Locate and identify every blood parasite.
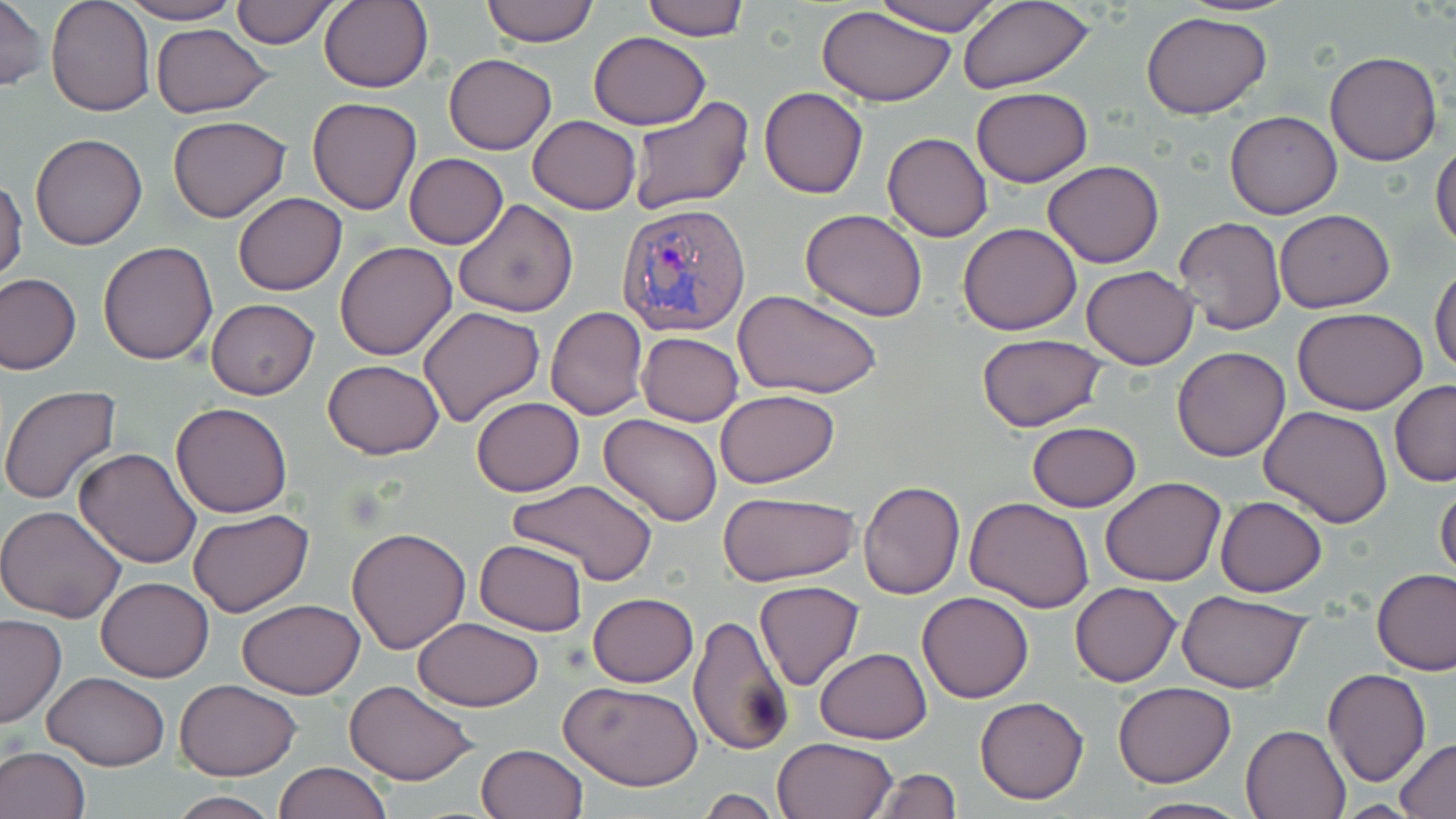
Approximate bounding boxes as [x1, y1, x2, y2] in pixels.
Plasmodium vivax-infected red blood cells: [616, 203, 752, 339].
No Plasmodium falciparum, Plasmodium ovale, Plasmodium malariae, Babesia divergens, or Trypanosoma brucei observed.

Uninfected red blood cell locations: [0, 0, 48, 95], [46, 0, 154, 117], [230, 0, 338, 48], [319, 0, 433, 94], [481, 0, 599, 46], [867, 0, 1008, 36], [1173, 0, 1304, 17], [119, 1, 242, 24], [639, 1, 749, 41], [956, 2, 1097, 92], [817, 7, 956, 107], [1140, 11, 1273, 120], [149, 22, 274, 118], [588, 31, 710, 128], [1324, 51, 1442, 167], [444, 54, 557, 154], [759, 86, 868, 199], [970, 87, 1092, 187], [627, 95, 754, 215], [306, 97, 422, 214], [1224, 109, 1342, 219], [166, 115, 291, 222], [528, 116, 641, 214], [882, 131, 993, 242], [30, 133, 147, 249], [1431, 143, 1456, 251], [404, 153, 509, 249], [1043, 161, 1165, 267], [0, 175, 28, 285], [234, 192, 346, 295], [453, 199, 578, 318], [799, 209, 929, 321], [1275, 209, 1393, 310], [1173, 216, 1286, 335], [957, 223, 1083, 335], [334, 241, 457, 361], [97, 242, 219, 366], [1430, 264, 1456, 376], [1080, 265, 1198, 369], [0, 274, 81, 375], [735, 289, 882, 400], [206, 298, 319, 400], [417, 305, 545, 428], [546, 307, 647, 419], [1294, 307, 1428, 415], [637, 330, 744, 426], [976, 334, 1108, 431], [1172, 345, 1291, 461], [322, 359, 444, 459], [1389, 380, 1456, 486], [1, 385, 123, 505], [714, 390, 838, 489], [471, 397, 584, 495], [170, 401, 293, 518], [1260, 405, 1393, 528], [599, 414, 723, 527], [1027, 422, 1142, 512], [73, 447, 203, 568], [507, 477, 660, 587], [1100, 477, 1226, 587], [857, 480, 965, 599], [1435, 483, 1456, 583], [718, 491, 859, 585], [965, 496, 1094, 611], [1200, 496, 1318, 690], [1214, 496, 1327, 597], [0, 504, 128, 624], [187, 508, 313, 617], [347, 525, 472, 654], [474, 539, 589, 636], [1373, 570, 1455, 675], [95, 577, 215, 682], [754, 579, 865, 691], [1069, 580, 1182, 687], [1176, 590, 1312, 692], [917, 591, 1035, 703], [587, 592, 698, 686], [238, 600, 365, 699], [689, 613, 794, 756], [0, 614, 66, 727], [414, 617, 545, 710], [814, 648, 932, 744], [1323, 668, 1431, 786], [42, 671, 169, 770], [175, 679, 302, 780], [343, 680, 477, 784], [561, 681, 703, 790], [1112, 682, 1237, 786], [974, 696, 1089, 804], [1241, 724, 1350, 818], [772, 736, 898, 819], [1394, 737, 1456, 816], [476, 743, 587, 819], [0, 746, 92, 819], [275, 761, 390, 818], [869, 767, 961, 819], [695, 789, 785, 819], [166, 793, 281, 818], [1128, 796, 1252, 818]. Slide-level diagnosis: Plasmodium vivax. 1000x magnification. Thin blood film. One field of a larger specimen. May-Grünwald-Giemsa stain. Image is 1456×819 pixels. Optical microscopy.